Give the extent of all uninfected red blood cells.
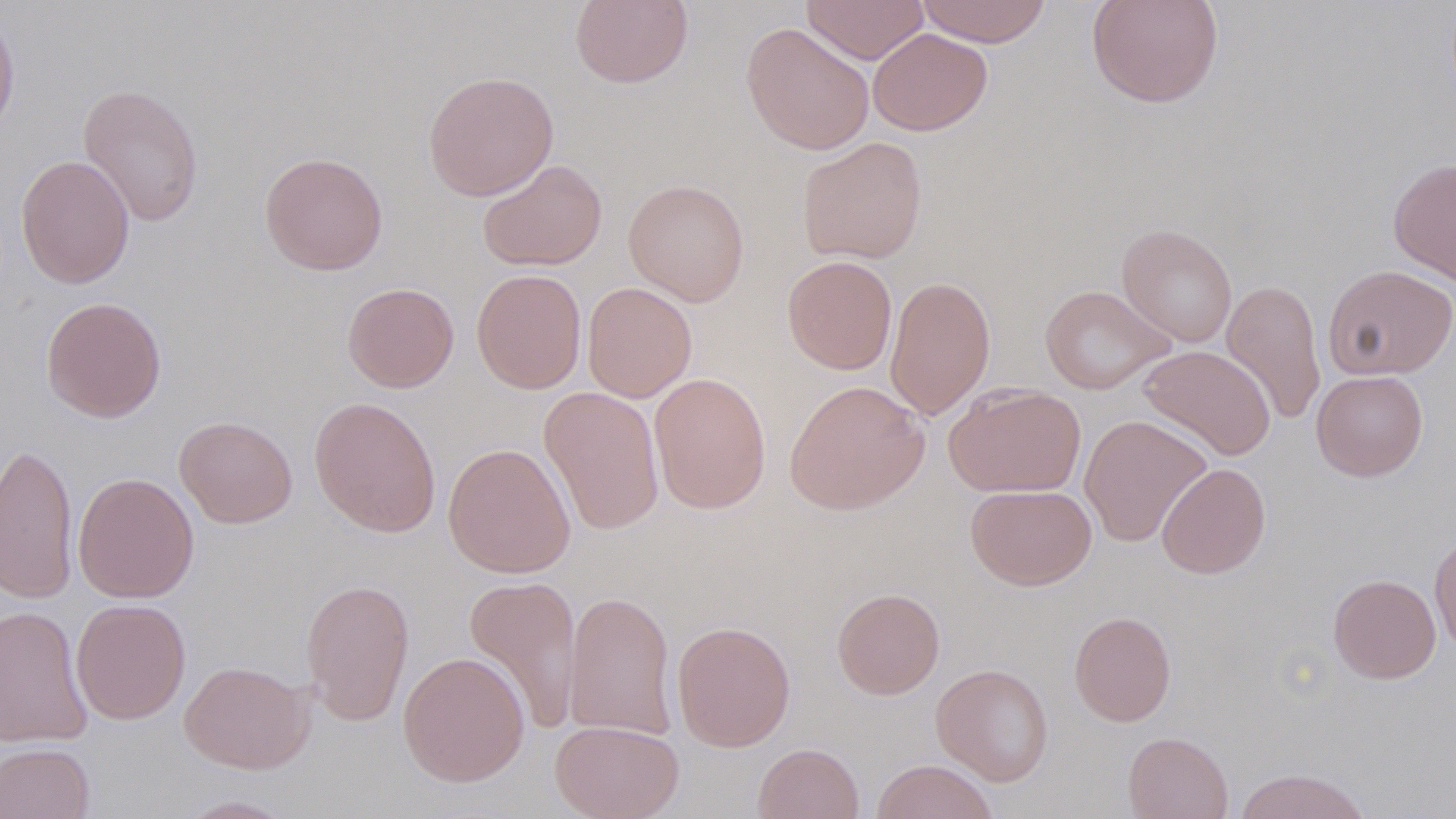
Approximate bounding boxes as [x1, y1, x2, y2] in pixels.
Uninfected red blood cells: [569, 0, 693, 89], [801, 0, 929, 64], [915, 0, 1052, 46], [1086, 0, 1224, 109], [0, 3, 20, 146], [740, 22, 875, 155], [868, 28, 993, 135], [423, 69, 559, 201], [77, 82, 204, 227], [797, 136, 928, 264], [259, 152, 388, 275], [15, 154, 135, 289], [1388, 157, 1456, 285], [477, 158, 608, 272], [623, 179, 750, 306], [1116, 223, 1238, 347], [782, 255, 898, 375], [1323, 264, 1456, 380], [471, 268, 587, 394], [884, 275, 996, 421], [1221, 279, 1326, 425], [343, 282, 459, 392], [582, 282, 697, 403], [1039, 285, 1176, 395], [41, 296, 167, 422], [1138, 344, 1276, 461], [1311, 370, 1428, 481], [648, 372, 772, 514], [784, 379, 929, 515], [944, 383, 1086, 497], [539, 386, 666, 537], [309, 395, 441, 538], [1079, 414, 1212, 547], [174, 415, 298, 528], [0, 441, 79, 604], [442, 443, 576, 579], [1156, 462, 1271, 579], [73, 472, 199, 603], [966, 484, 1097, 590], [1429, 533, 1456, 652], [1328, 573, 1441, 684], [464, 574, 583, 734], [301, 578, 414, 726], [831, 588, 945, 699], [563, 590, 677, 741], [71, 599, 191, 725], [0, 604, 93, 747], [1069, 610, 1176, 726], [672, 621, 796, 751], [398, 651, 530, 787], [179, 660, 313, 773], [931, 664, 1054, 786], [550, 720, 684, 819], [1122, 731, 1233, 819], [0, 742, 95, 819], [752, 742, 864, 819], [871, 759, 998, 819], [1233, 767, 1372, 819], [174, 795, 297, 818].

slide-level diagnosis = negative for blood parasites
field of view = one of a larger specimen
preparation = thin blood smear
magnification = 1000x
modality = optical microscopy
stain = May-Grünwald-Giemsa
image size = 1456×819 pixels